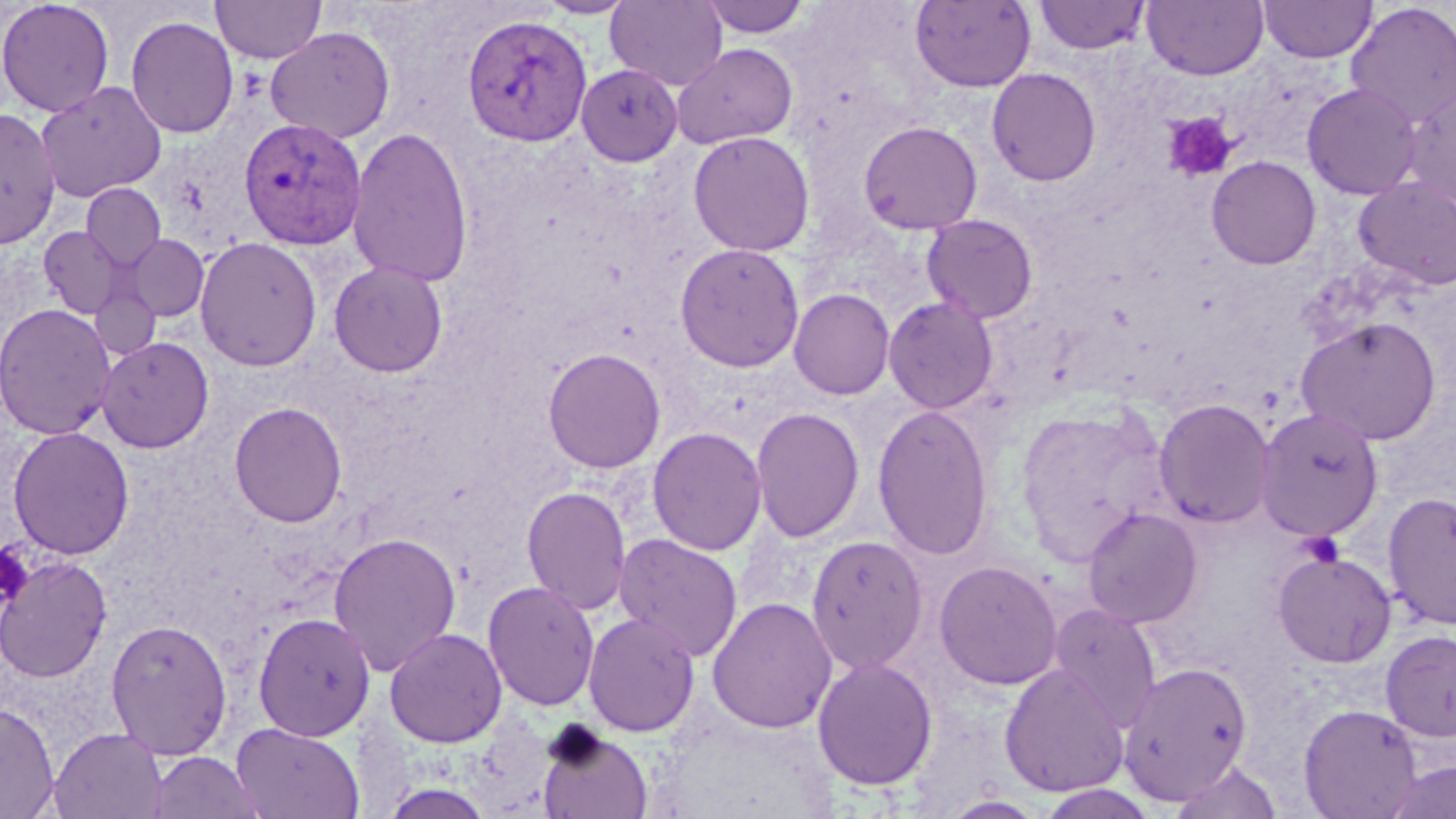
Approximate bounding boxes as (x1,y1)-(x2,y2) corner pairs in pixels. Platelet locations: (1163,112)-(1238,182), (1299,532)-(1344,568), (0,541)-(31,610). Plasmodium vivax-infected red blood cell locations: (461,13)-(593,147), (237,116)-(367,251). Uninfected red blood cell locations: (0,0)-(115,117), (211,0)-(327,65), (535,0)-(637,19), (606,0)-(728,90), (697,0)-(813,38), (910,0)-(1036,93), (1034,0)-(1151,55), (1142,0)-(1269,80), (1259,0)-(1377,63), (1345,2)-(1456,129), (126,15)-(239,139), (265,27)-(395,143), (672,43)-(798,149), (576,64)-(682,166), (986,67)-(1101,187), (36,80)-(167,202), (1302,82)-(1423,199), (1401,83)-(1456,207), (0,106)-(61,249), (858,121)-(983,235), (347,125)-(474,288), (687,131)-(815,257), (1206,156)-(1321,269), (1353,176)-(1456,291), (81,184)-(166,271), (921,214)-(1038,324), (39,226)-(124,318), (123,234)-(209,321), (194,236)-(322,371), (674,242)-(805,373), (328,260)-(448,377), (89,279)-(162,361), (788,288)-(895,400), (883,297)-(999,414), (0,303)-(117,439), (1295,315)-(1442,445), (96,336)-(214,453), (542,347)-(666,474), (1153,398)-(1276,529), (228,401)-(347,527), (872,404)-(994,561), (1016,404)-(1172,567), (750,407)-(866,543), (1256,408)-(1384,542), (7,426)-(135,560), (647,426)-(767,556), (521,486)-(632,615), (1383,491)-(1456,631), (1082,507)-(1203,628), (328,531)-(461,676), (613,533)-(743,663), (806,534)-(929,675), (1272,550)-(1396,667), (0,556)-(112,684), (933,559)-(1063,690), (482,580)-(600,712), (707,596)-(838,734), (1048,604)-(1162,730), (252,611)-(376,741), (583,612)-(701,737), (105,618)-(233,760), (384,627)-(508,747), (1380,630)-(1456,743), (812,657)-(939,791), (1118,661)-(1253,804), (999,664)-(1129,798), (0,701)-(59,819), (1298,704)-(1422,818), (650,710)-(839,819), (230,721)-(364,819), (535,724)-(654,819), (49,727)-(167,818), (148,750)-(264,819), (1169,759)-(1284,819), (1384,760)-(1456,819), (1034,783)-(1158,819), (939,794)-(1048,818). Slide-level diagnosis: Plasmodium vivax. Optical microscopy. May-Grünwald-Giemsa stain. One field of a larger specimen. Thin blood film. 1000x magnification. Image is 1456×819 pixels.